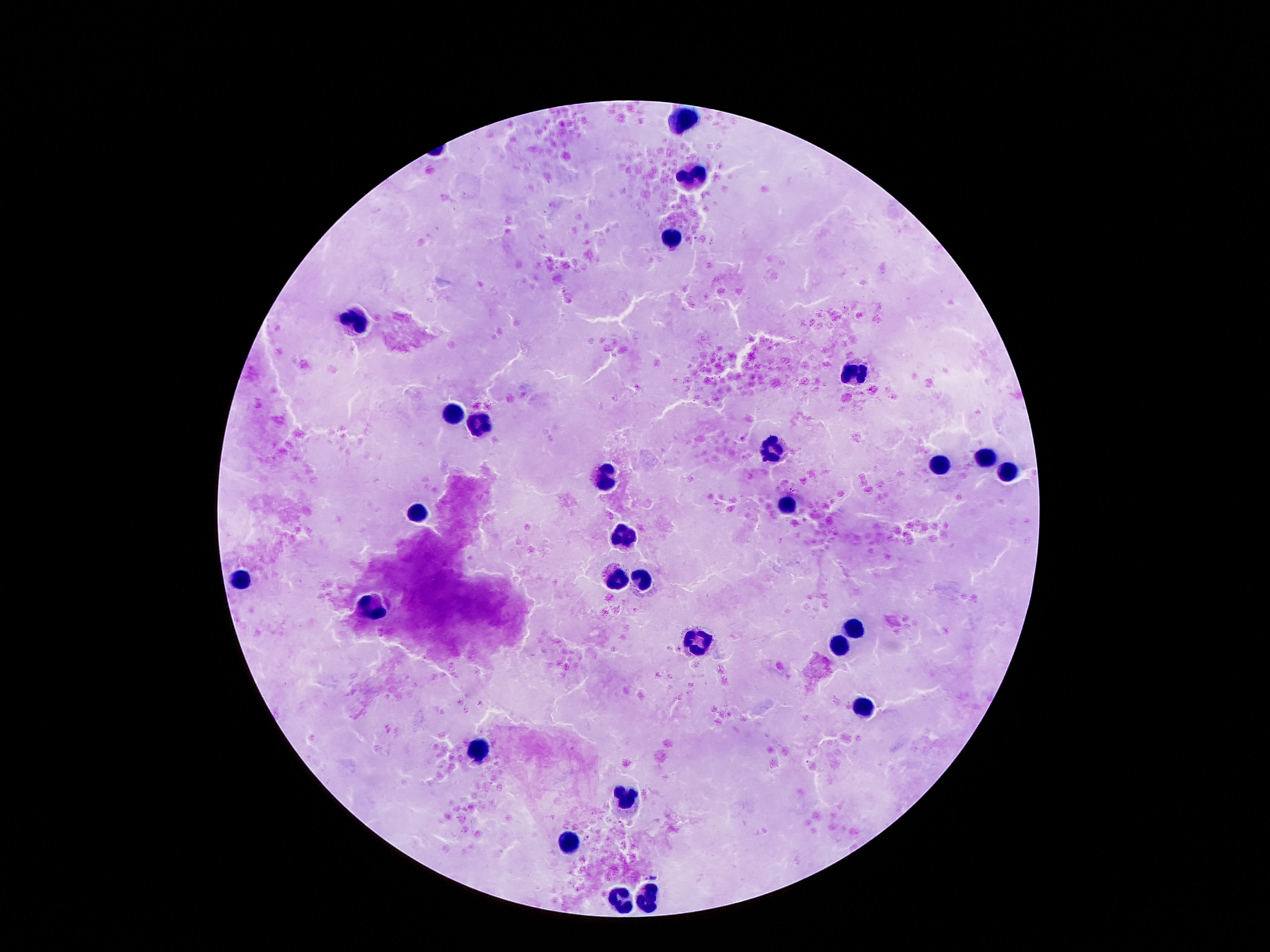

capture = smartphone camera through the microscope eyepiece
leukocyte locations = approximate centers as [x, y] in pixels: [680, 118], [692, 177], [671, 238], [356, 322], [854, 372], [453, 412], [478, 425], [772, 454], [984, 456], [940, 465], [1007, 471], [608, 475], [787, 510], [417, 513], [621, 537], [615, 577], [241, 579], [640, 580], [371, 605], [854, 628], [699, 645], [837, 649], [865, 708], [476, 748], [627, 800], [568, 844], [650, 896], [621, 898]
magnification = 100x
stain = Giemsa
patient malaria status = negative
field of view = one from this slide
image size = 1270×952 pixels
preparation = thick blood film